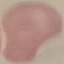

result = no malaria parasites detected
preparation = thin blood smear
capture = smartphone through the microscope eyepiece
image type = cell patch, automatically extracted from a larger field of view and resized to 64 × 64 pixels
stain = Giemsa